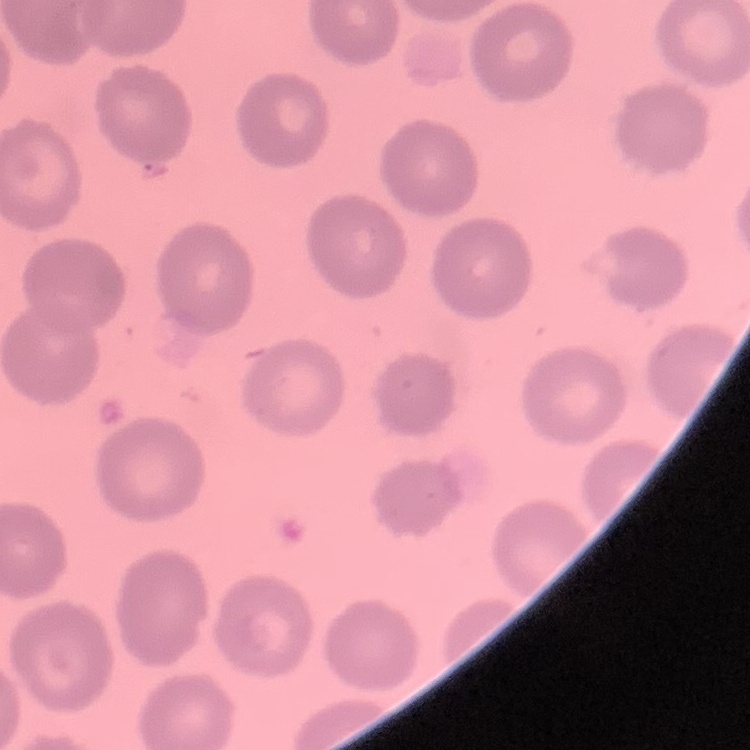
erythrocyte morphology = no rouleaux formation
stain = Field's or Giemsa
preparation = thin blood film
image type = square crop of a larger photomicrograph